Assess this cell for malaria.
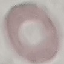
Uninfected.

capture: smartphone camera at the microscope eyepiece
stain: Giemsa
preparation: thin blood film
image_type: cell patch, automatically extracted from a larger field of view and resized to 64 × 64 pixels